Identify the parasite.
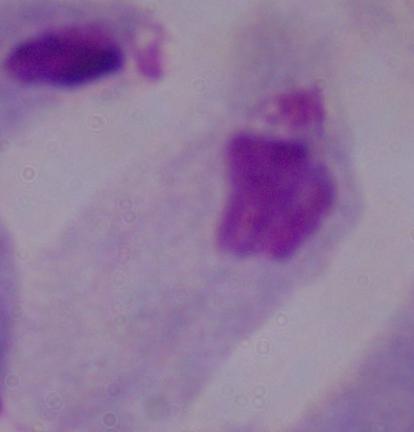
A trichomonad.

Summary:
  - Modality: micrograph
  - Magnification: 1000x